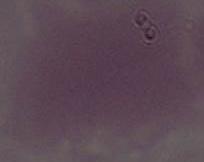

Summary:
  - Modality: micrograph
  - Identification: erythrocyte
  - Magnification: 1000x